Outline each Plasmodium falciparum parasite and classify it by life-cycle stage.
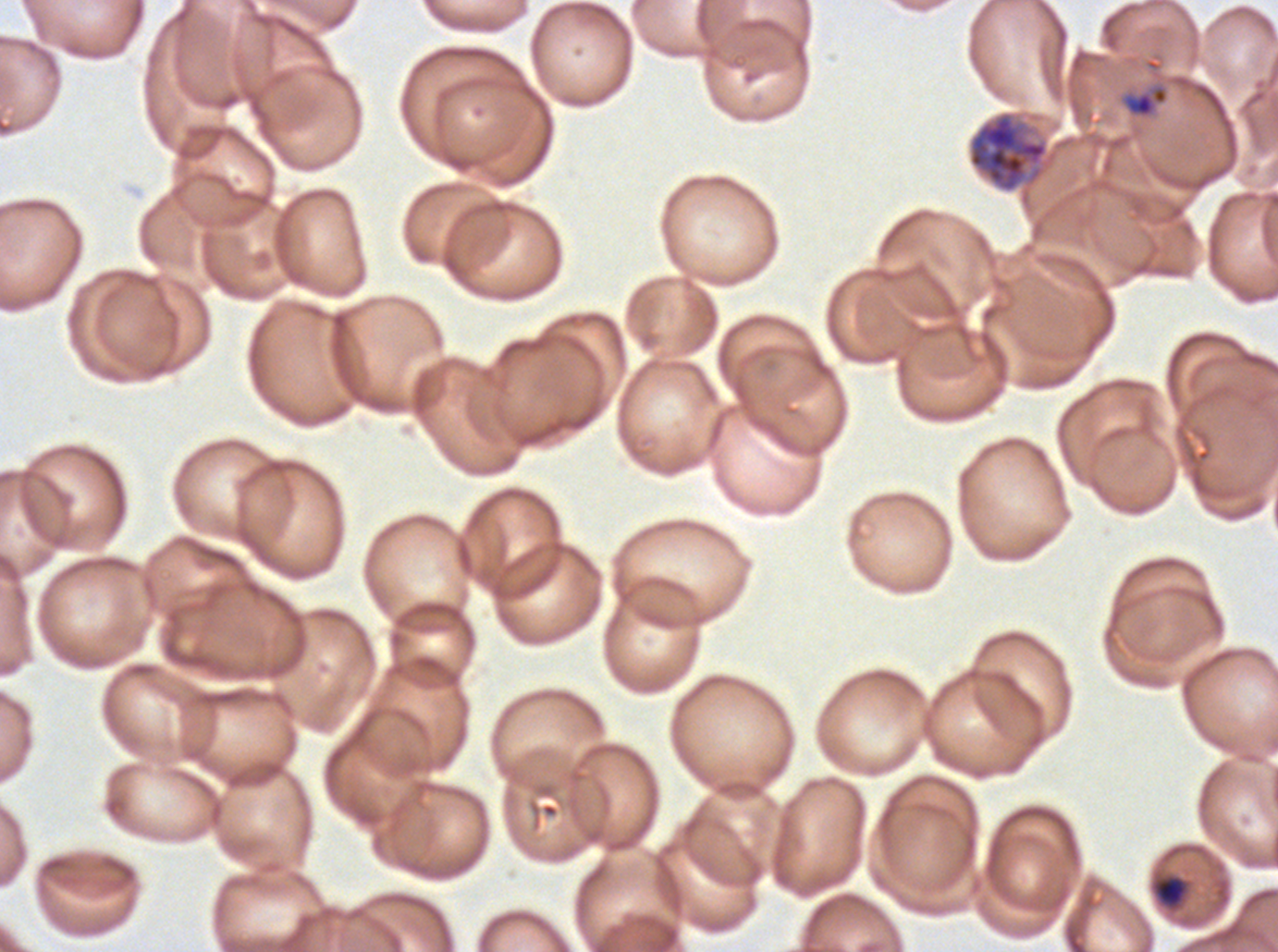

Approximate bounding boxes as (x1, y1, x2, y2) in pixels.
Late-ring/early-trophozoite forms: (1121, 82, 1169, 119).
Mid trophozoites: (1150, 873, 1189, 910).
Early schizonts: (967, 110, 1049, 193).
No rings, late trophozoites, late schizonts, segmenters, or gametocytes observed.

Giemsa stain. Life-cycle stages observed: late-ring/early-trophozoite, mid trophozoite, early schizont. Image is 1278×952 pixels. Thin blood smear. A sub-image separated from a larger composite. Plasmodium falciparum from a patient in The Gambia, cultured ex vivo for 24 to 48 hours.